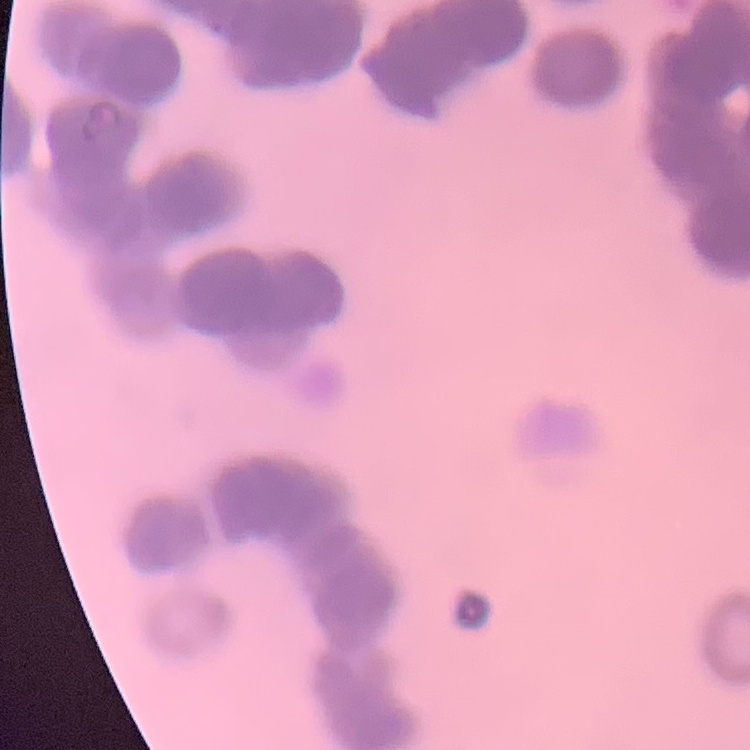

red_blood_cell_morphology: rouleaux formation
preparation: thin blood smear
stain: Field's or Giemsa
image_type: one tile cut from a larger photomicrograph